Report the malaria status of this cell.
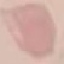
It is uninfected.

image type = automatically extracted cell patch, resized to 64 × 64 pixels
capture = smartphone through the microscope eyepiece
stain = Giemsa
preparation = thin blood film